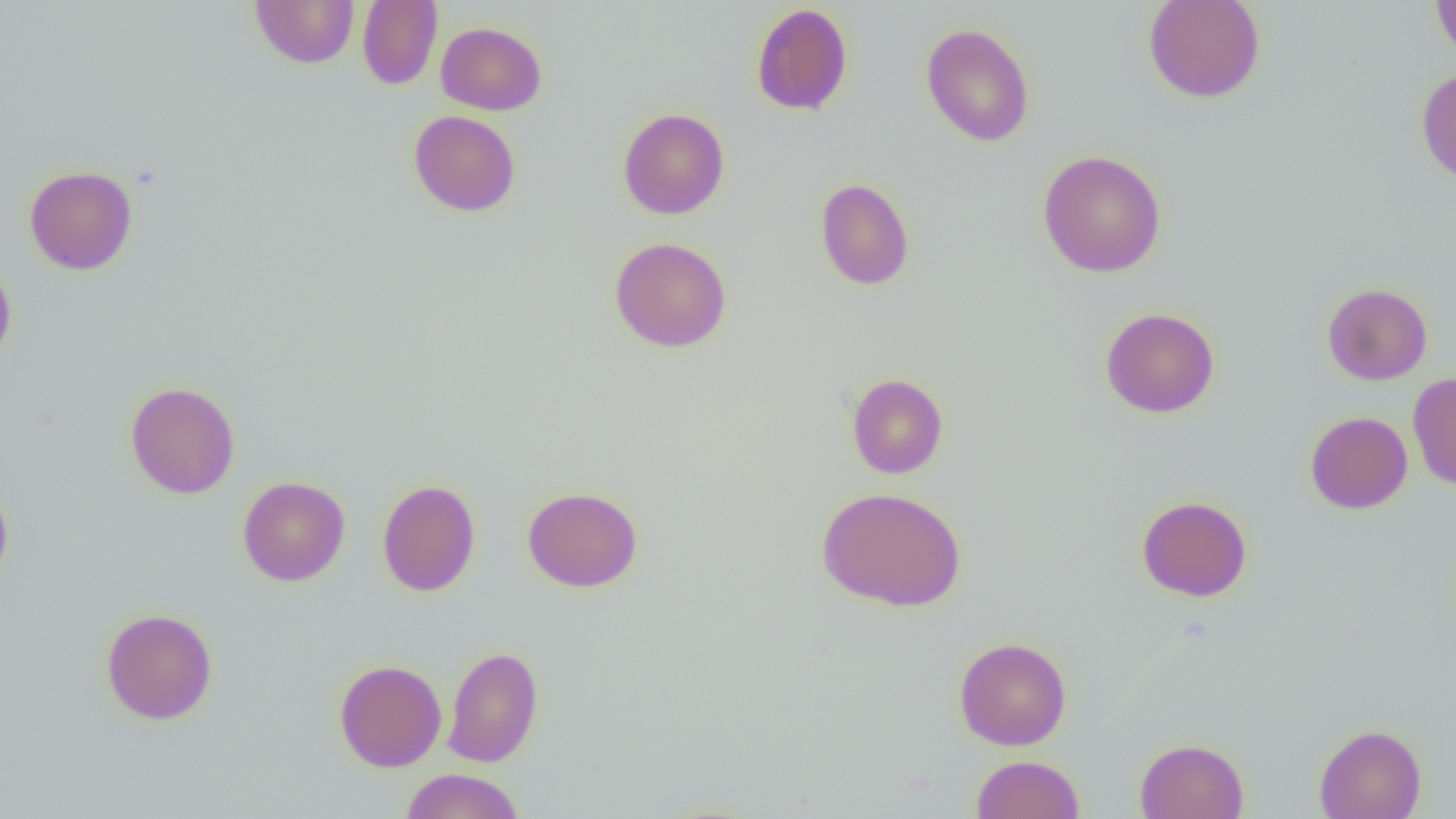

Summary:
  - Coordinate format: approximate bounding boxes as (x1,y1)-(x2,y2) corner pairs in pixels
  - Uninfected red blood cell locations: (250,0)-(360,68), (357,0)-(442,89), (1142,0)-(1266,103), (1431,0)-(1456,61), (751,3)-(853,117), (436,21)-(546,115), (920,23)-(1035,147), (1416,67)-(1456,185), (618,107)-(730,219), (408,110)-(521,216), (1037,149)-(1167,277), (24,165)-(138,275), (815,178)-(915,291), (609,237)-(732,352), (0,256)-(17,368), (1322,283)-(1432,385), (1099,307)-(1220,418), (1407,372)-(1456,490), (847,373)-(948,479), (125,381)-(240,499), (1305,411)-(1413,514), (0,476)-(14,587), (238,476)-(350,586), (377,479)-(481,597), (522,485)-(643,592), (816,486)-(967,612), (1136,495)-(1252,602), (101,607)-(218,724), (954,636)-(1072,750), (442,645)-(543,767), (334,659)-(446,772), (1314,724)-(1427,819), (1135,738)-(1249,819), (971,754)-(1085,819), (400,768)-(524,819)
  - Slide-level diagnosis: no evidence of blood parasites
  - Modality: light microscopy
  - Preparation: thin blood smear
  - Magnification: 1000x
  - Image size: 1456×819 pixels
  - Field of view: one of a larger specimen